Draw a bounding box around every malaria parasite.
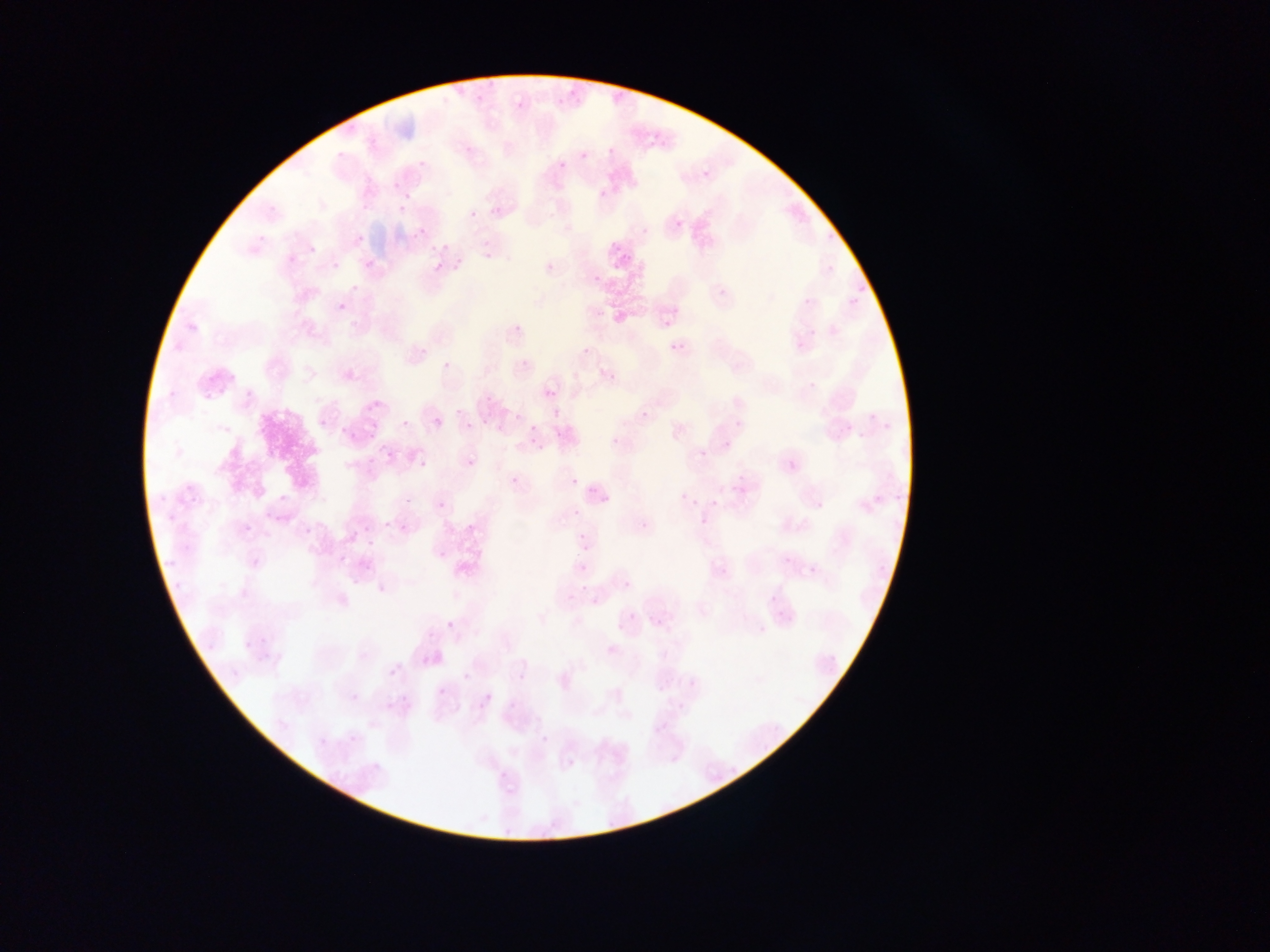

Approximate bounding boxes as [left, top, right, bottom] in pixels.
Malaria parasites: [515, 99, 526, 111], [652, 131, 663, 143], [391, 180, 401, 191], [397, 204, 407, 214], [470, 209, 481, 222], [469, 210, 478, 219], [675, 215, 689, 237], [674, 219, 684, 230], [413, 229, 424, 239], [476, 248, 488, 263], [543, 258, 558, 275], [364, 259, 376, 272], [333, 261, 341, 270], [434, 262, 445, 273], [350, 283, 359, 292], [338, 303, 348, 313], [660, 305, 682, 329], [669, 341, 684, 356], [582, 346, 592, 357], [442, 360, 452, 371], [602, 368, 617, 384], [546, 388, 556, 399], [640, 408, 651, 421], [434, 417, 444, 428], [318, 418, 328, 429], [401, 419, 410, 429], [465, 421, 474, 430], [530, 424, 538, 432], [342, 425, 353, 439], [497, 425, 506, 434], [363, 432, 380, 445], [612, 435, 622, 447], [411, 445, 427, 470], [699, 448, 709, 459], [383, 450, 394, 461], [465, 457, 477, 469], [510, 476, 519, 485], [570, 477, 580, 488], [572, 479, 589, 491], [278, 494, 288, 504], [709, 498, 720, 509], [382, 520, 392, 531], [638, 520, 651, 534], [398, 523, 410, 535], [243, 525, 254, 536], [578, 533, 591, 546], [366, 539, 375, 549], [578, 539, 592, 554], [437, 549, 450, 563], [577, 562, 589, 574], [769, 593, 779, 604], [445, 620, 455, 631], [241, 637, 253, 651], [389, 668, 398, 677], [462, 672, 471, 681], [437, 687, 447, 698], [352, 693, 361, 703], [481, 693, 493, 706], [402, 696, 411, 705], [385, 702, 395, 712], [346, 732, 362, 748], [565, 757, 577, 771].

Summary:
  - Preparation: thin blood smear
  - Field of view: single
  - Image size: 1270×952 pixels
  - Country: Ghana
  - Capture: mobile-phone photograph through a microscope